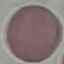

malaria status = uninfected
stain = Giemsa
preparation = thin blood smear
capture = smartphone camera at the microscope eyepiece
image type = automatically extracted cell patch, resized to 64 × 64 pixels